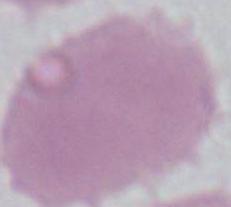

1000x magnification. Micrograph. An erythrocyte is seen.